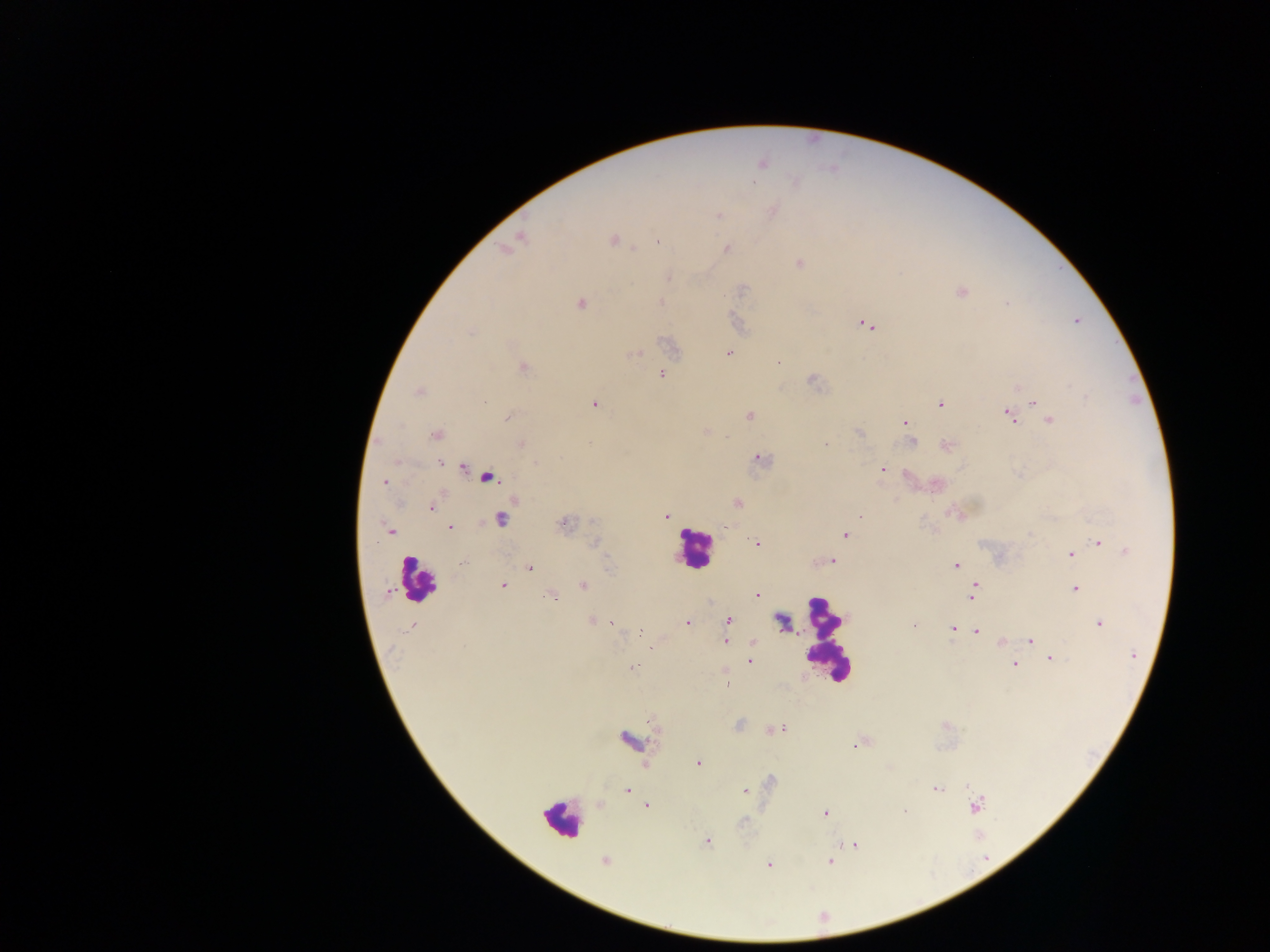

image size = 1270×952 pixels
field of view = single
country = Ghana
malaria parasite locations = approximate centers as [x, y] in pixels: [761, 163], [772, 211], [718, 215], [517, 239], [613, 240], [656, 241], [507, 247], [726, 249], [798, 263], [668, 278], [961, 292], [661, 301], [580, 304], [1076, 321], [865, 324], [728, 352], [633, 354], [778, 361], [522, 367], [660, 374], [813, 380], [1020, 386], [419, 391], [1032, 401], [940, 403], [595, 404], [1008, 413], [749, 416], [507, 417], [1049, 419], [905, 424], [705, 432], [859, 432], [436, 434], [911, 441], [520, 444], [947, 445], [758, 458], [440, 462], [462, 464], [882, 469], [486, 476], [385, 482], [934, 484], [736, 503], [432, 507], [861, 515], [666, 517], [500, 519], [563, 524], [448, 528], [390, 531], [844, 534], [1098, 541], [757, 543], [1125, 551], [1070, 553], [831, 562], [955, 565], [529, 567], [583, 584], [502, 585], [975, 586], [1074, 589], [552, 595], [758, 596], [972, 597], [591, 620], [781, 620], [728, 621], [611, 623], [686, 623], [1099, 623], [914, 624], [413, 625], [954, 629], [975, 631], [638, 633], [1030, 639], [726, 641], [1001, 641], [751, 642], [1049, 658], [749, 660], [1014, 662], [632, 668], [725, 672], [775, 729], [630, 740], [855, 745], [698, 762], [645, 765], [936, 788], [627, 789], [744, 790], [646, 804], [601, 805], [974, 805], [905, 812], [826, 813], [707, 840], [853, 844], [604, 861], [830, 862], [768, 864]
capture = mobile-phone photograph through a microscope
leukocyte locations = approximate centers as [x, y] in pixels: [694, 548], [417, 578], [825, 644], [561, 819]
preparation = thick blood smear